Describe the morphology of the erythrocytes.
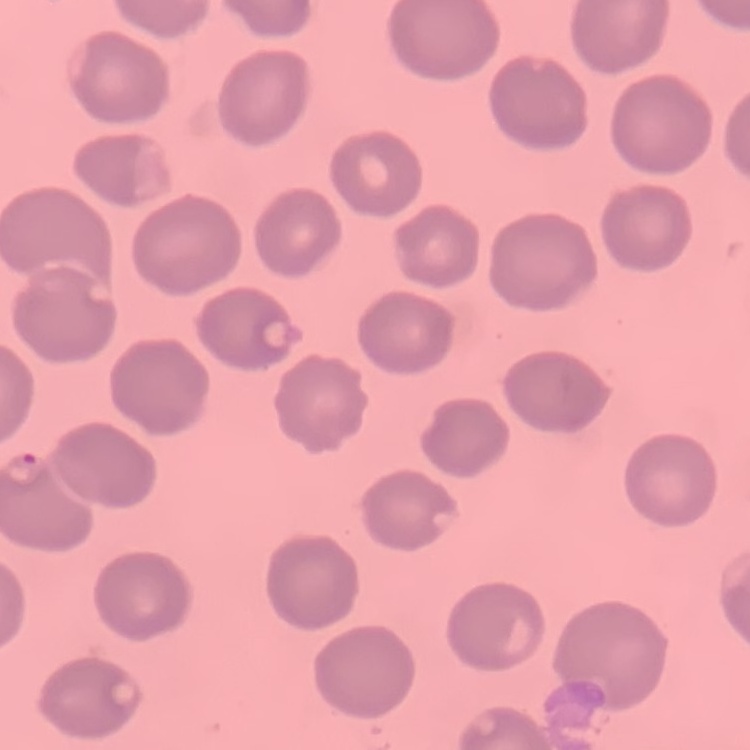

No rouleaux formation.

stain = Field's or Giemsa
preparation = thin peripheral smear
image type = square crop of a larger photomicrograph